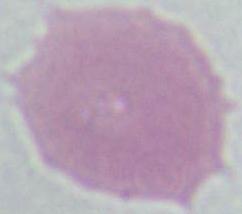

magnification: 1000x
modality: photomicrograph
identification: red blood cell